Give a bounding box for every leukocyte visible.
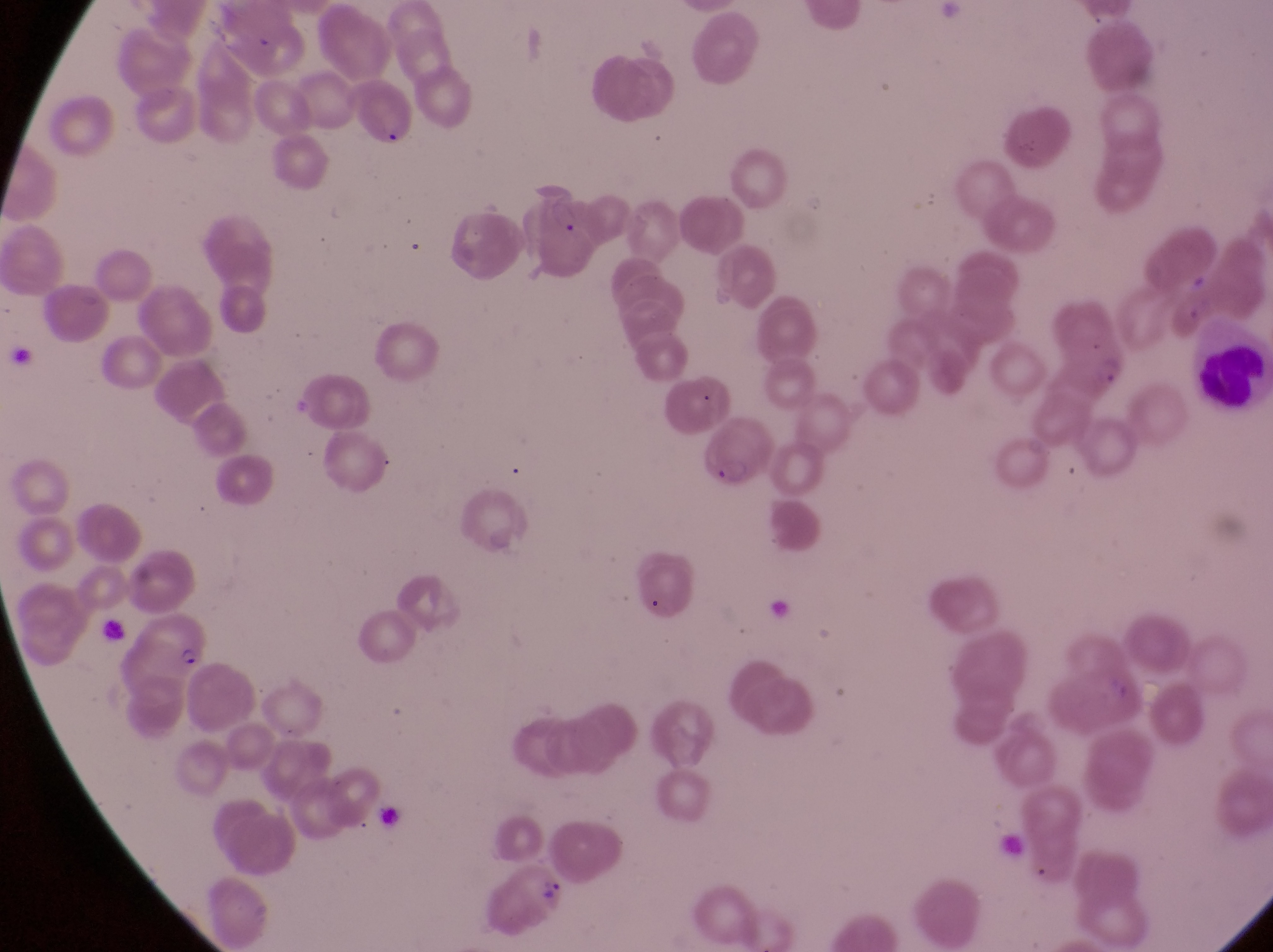
Approximate bounding boxes as [left, top, right, bottom] in pixels.
Leukocytes: [1186, 330, 1264, 427].

Summary:
  - Parasitised red blood cell locations: [355, 84, 416, 154], [533, 188, 596, 280], [699, 427, 756, 495], [132, 609, 207, 679], [500, 864, 587, 922]
  - Trophozoite locations: [1096, 355, 1133, 395]
  - Preparation: thin blood film
  - Country: Uganda
  - Field of view: single
  - Capture: smartphone photograph through the eyepiece of an Olympus CX-23 microscope
  - Image size: 1273×952 pixels
  - Magnification: 1000x